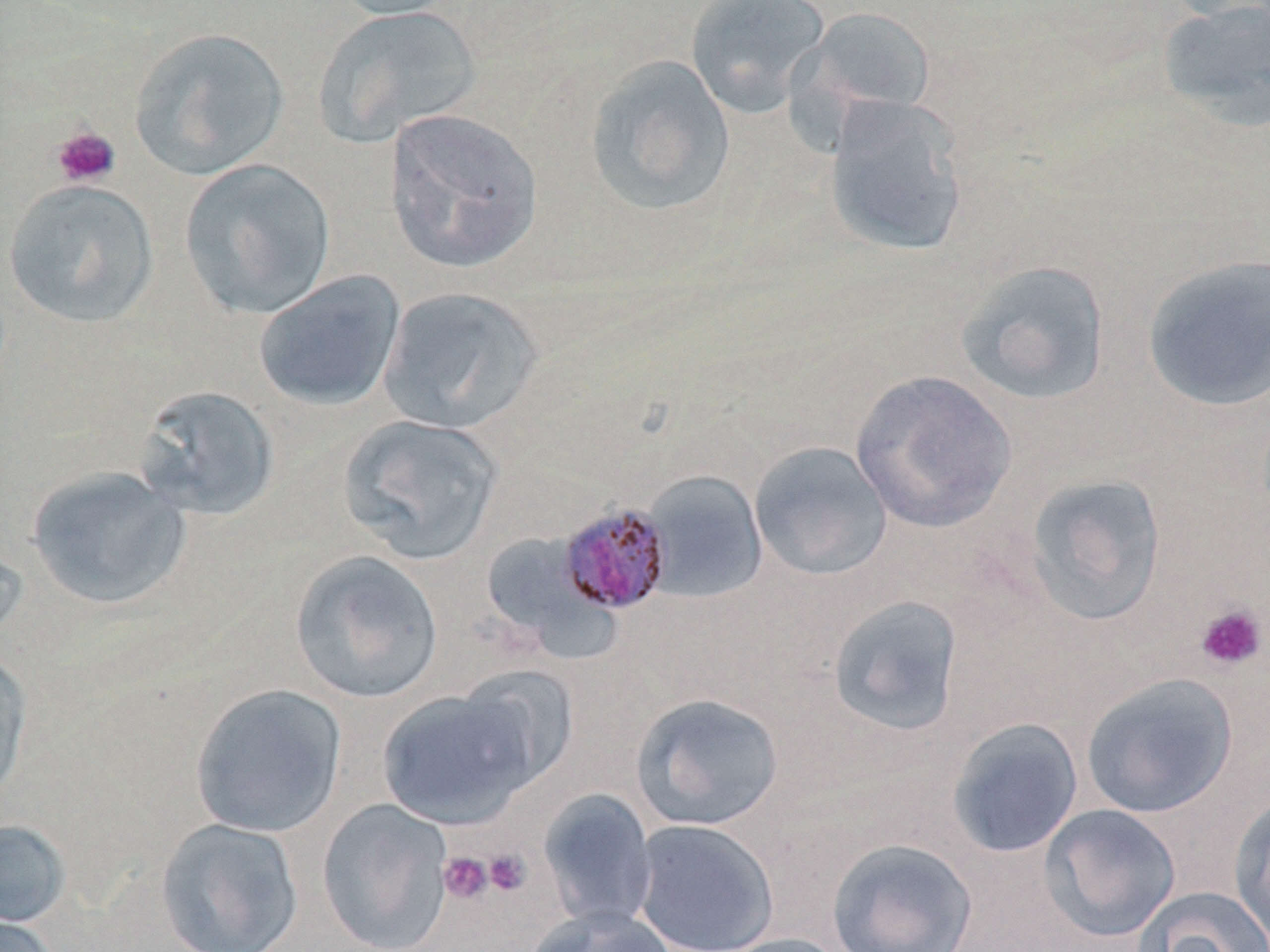
slide-level diagnosis = Plasmodium malariae
stain = May-Grünwald-Giemsa
preparation = thin blood smear
platelet locations = approximate bounding boxes as [x1, y1, x2, y2] in pixels: [51, 126, 121, 187], [1195, 603, 1267, 672], [483, 848, 531, 896], [438, 852, 494, 905]
image size = 1270×952 pixels
field of view = single
uninfected red blood cell locations = approximate bounding boxes as [x1, y1, x2, y2] in pixels: [326, 0, 465, 21], [685, 0, 830, 118], [1155, 0, 1270, 132], [1160, 0, 1270, 23], [311, 5, 482, 148], [800, 5, 937, 117], [128, 27, 290, 181], [583, 54, 736, 217], [821, 95, 971, 258], [383, 107, 544, 275], [178, 159, 336, 319], [2, 178, 160, 328], [1141, 254, 1270, 413], [955, 259, 1112, 406], [253, 270, 405, 412], [377, 286, 544, 434], [849, 368, 1017, 534], [132, 384, 282, 521], [336, 414, 505, 564], [749, 441, 893, 581], [25, 465, 192, 610], [640, 470, 769, 604], [1022, 471, 1167, 628], [491, 531, 624, 665], [0, 537, 28, 649], [289, 549, 444, 704], [826, 594, 965, 737], [0, 647, 33, 805], [454, 664, 580, 791], [1080, 672, 1238, 818], [189, 683, 347, 838], [377, 687, 536, 829], [630, 692, 785, 831], [946, 717, 1084, 859], [538, 787, 658, 932], [1229, 794, 1270, 944], [316, 798, 454, 952], [1038, 803, 1181, 942], [155, 817, 304, 952], [631, 818, 780, 952], [0, 819, 72, 928], [826, 837, 978, 952], [1132, 885, 1270, 952], [526, 906, 678, 952], [0, 914, 63, 952], [713, 933, 852, 952]
modality = light microscopy
Plasmodium malariae-infected red blood cell locations = approximate bounding boxes as [x1, y1, x2, y2] in pixels: [558, 502, 675, 615]
magnification = 1000x